Report the malaria status of this cell.
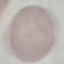

It is uninfected.

preparation = thin blood smear
image type = cell patch, automatically extracted from a larger field of view and resized to 64 × 64 pixels
stain = Giemsa
capture = smartphone camera at the microscope eyepiece